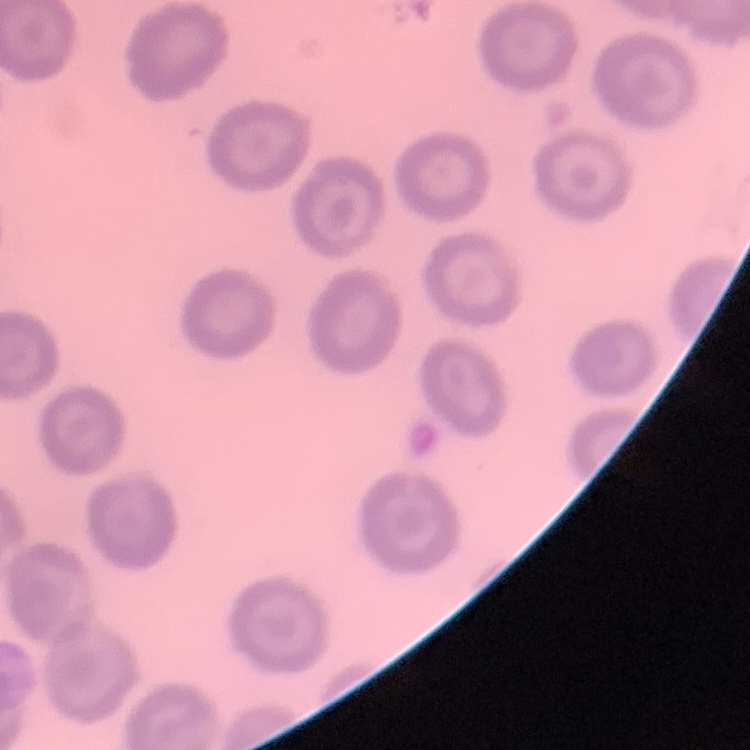
The erythrocytes exhibit no rouleaux formation. Square crop of a larger photomicrograph. Stained with either Field's or Giemsa. Thin blood smear.